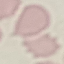

Result: negative for malaria parasites. Giemsa stain. Photographed with a smartphone camera at the microscope eyepiece. Thin blood smear. Automatically extracted cell patch, resized to 64 × 64 pixels.